Comment on the morphology of the erythrocytes.
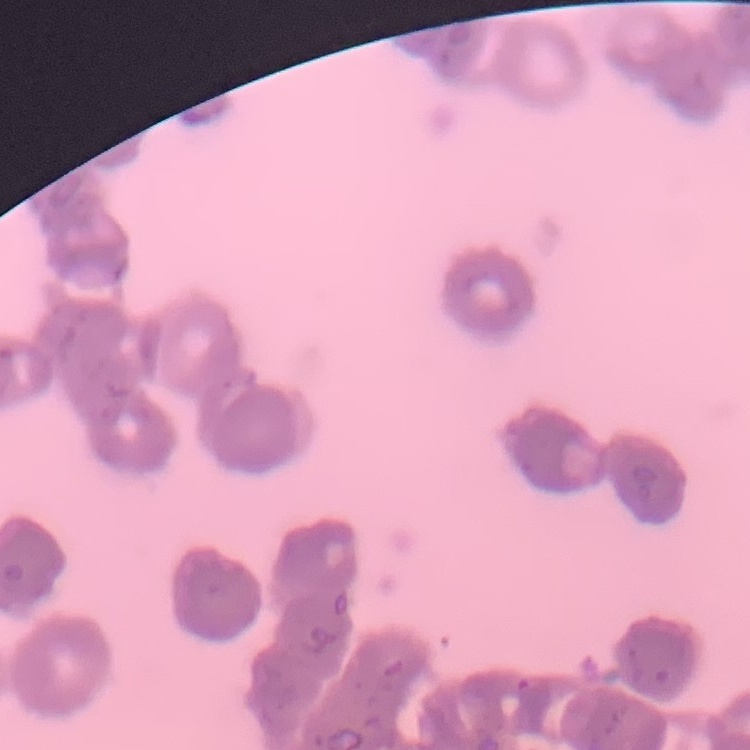

They show rouleaux formation.

Summary:
  - Image type: one tile cut from a larger photomicrograph
  - Preparation: thin blood film
  - Stain: Field's or Giemsa